Classify this cell by malaria status.
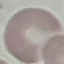
It is uninfected.

Summary:
  - Preparation: thin blood film
  - Stain: Giemsa
  - Image type: cell patch, automatically extracted from a larger field of view and resized to 64 × 64 pixels
  - Capture: smartphone through the microscope eyepiece